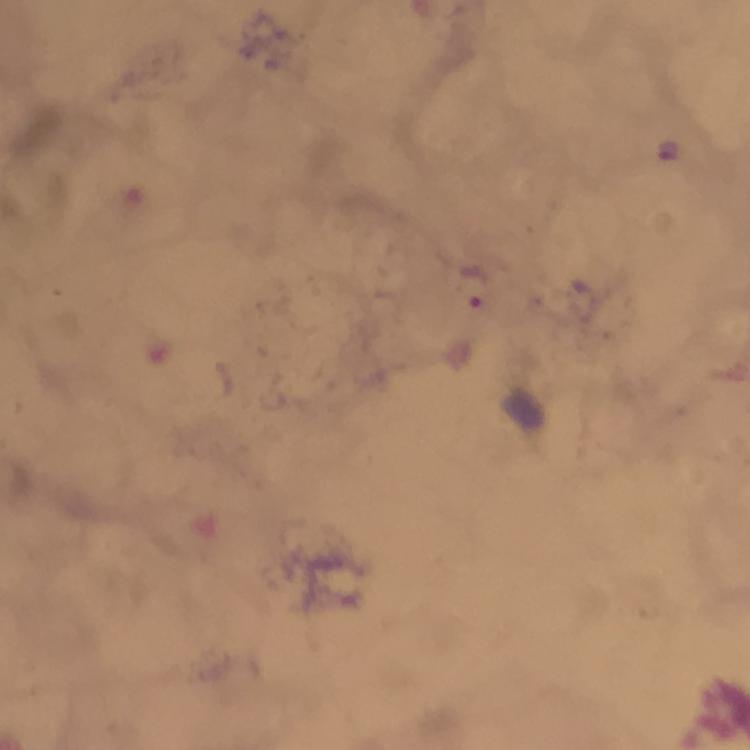

Approximate centers as (x, y) in pixels. Plasmodium parasite locations: (667, 149), (474, 285). Smartphone photograph taken through a microscope. A crop from one field of view. Immersion oil was used. 100x magnification. Giemsa stain. Image is 750×750 pixels. From a diagnostic examination for malaria. Thick blood smear.